State which parasite is depicted.
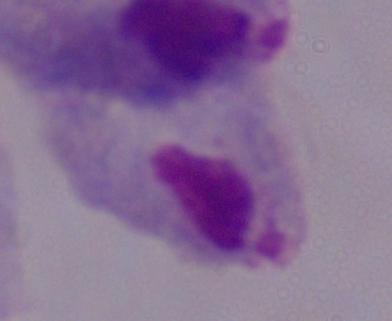
This is a trichomonad.

Summary:
  - Magnification: 1000x
  - Modality: photomicrograph